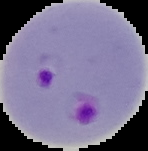
{
  "malaria_status": "parasitized",
  "image_size": "148×151 pixels",
  "preparation": "thin blood smear",
  "image_type": "segmented cell region on a black background"
}